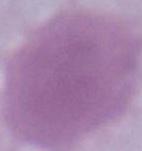

modality = micrograph
magnification = 1000x
identification = red blood cell